State which parasite is depicted.
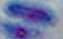

Toxoplasma gondii.

modality = photomicrograph
magnification = 1000x